Report the malaria status of this cell.
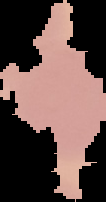
Uninfected.

Summary:
  - Image type: segmented cell region on a black background
  - Preparation: thin blood smear
  - Image size: 106×202 pixels